Outline each blood parasite and name the species.
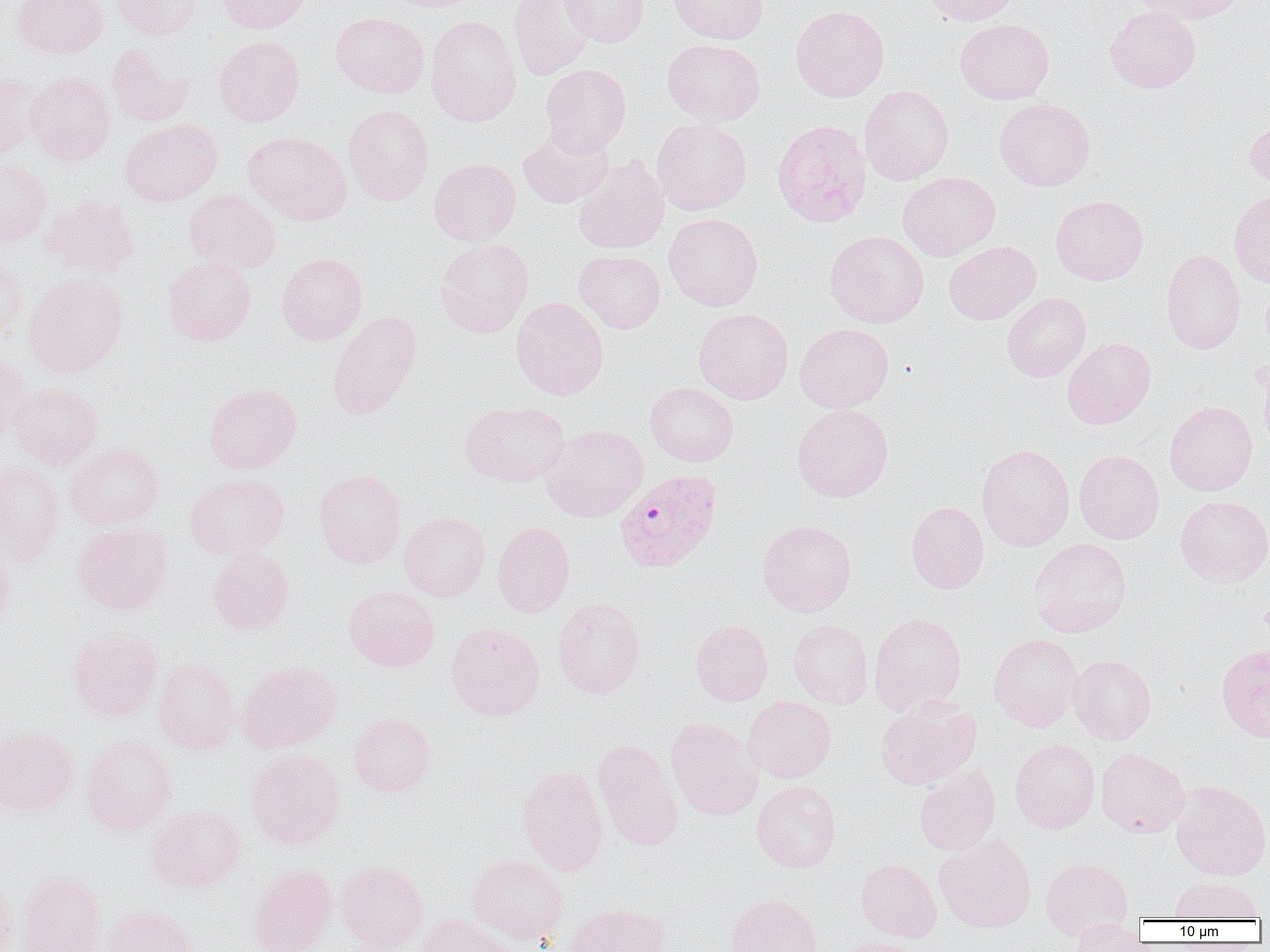
Approximate bounding boxes as (x1,y1)-(x2,y2) corner pairs in pixels.
Plasmodium falciparum-infected red blood cells: (615,469)-(722,573).
No Plasmodium ovale, Plasmodium malariae, Plasmodium vivax, Babesia divergens, or Trypanosoma brucei observed.

Uninfected red blood cell locations: (12,0)-(109,58), (112,0)-(203,40), (214,0)-(312,33), (378,0)-(481,12), (509,0)-(597,80), (560,0)-(650,47), (669,0)-(769,44), (919,0)-(1020,26), (1131,0)-(1248,24), (790,5)-(890,102), (1104,6)-(1201,93), (330,12)-(428,98), (425,15)-(521,126), (955,19)-(1054,104), (214,36)-(304,126), (662,38)-(765,126), (107,43)-(193,127), (540,63)-(631,156), (25,72)-(115,166), (0,73)-(44,160), (859,84)-(954,185), (994,97)-(1095,191), (343,104)-(434,205), (1244,115)-(1270,193), (119,118)-(222,206), (771,118)-(871,228), (652,119)-(752,215), (243,131)-(352,225), (517,131)-(614,208), (573,156)-(670,254), (429,158)-(521,246), (0,159)-(51,248), (897,171)-(1000,261), (183,189)-(281,275), (1229,192)-(1270,288), (41,195)-(139,278), (1050,195)-(1148,285), (664,213)-(763,311), (824,230)-(929,328), (434,238)-(534,337), (944,241)-(1041,324), (1161,249)-(1246,354), (574,250)-(665,333), (0,252)-(27,341), (276,252)-(367,344), (163,256)-(256,346), (23,272)-(128,378), (1002,292)-(1091,381), (511,296)-(609,400), (694,308)-(793,404), (326,310)-(423,420), (794,323)-(894,413), (1062,337)-(1156,429), (0,351)-(32,444), (1257,355)-(1270,459), (204,382)-(302,474), (645,382)-(739,466), (9,383)-(102,469), (460,400)-(569,486), (1164,401)-(1258,496), (792,403)-(894,502), (540,424)-(649,521), (67,443)-(164,529), (976,444)-(1075,551), (1074,449)-(1164,544), (0,460)-(65,566), (314,468)-(407,569), (185,473)-(290,560), (1175,495)-(1270,585), (905,501)-(989,594), (399,512)-(491,601), (757,519)-(857,616), (493,521)-(575,617), (72,522)-(172,615), (0,538)-(15,634), (1029,538)-(1132,637), (208,547)-(294,635), (344,586)-(440,671), (551,597)-(646,699), (868,612)-(967,714), (690,619)-(773,705), (788,619)-(873,708), (446,622)-(545,720), (68,627)-(164,721), (988,633)-(1082,731), (1216,643)-(1270,743), (1068,654)-(1156,744), (153,657)-(240,755), (235,660)-(342,753), (743,696)-(837,783), (875,697)-(982,791), (349,713)-(435,796), (664,717)-(763,820), (0,727)-(78,817), (80,735)-(177,835), (592,738)-(684,851), (1010,738)-(1100,833), (1095,747)-(1190,837), (246,749)-(345,848), (914,763)-(1001,856), (517,765)-(608,876), (751,780)-(841,872), (1170,780)-(1270,880), (147,806)-(246,893), (934,833)-(1037,933), (467,854)-(568,943), (1040,857)-(1133,941), (855,859)-(942,942), (336,861)-(429,952), (248,863)-(337,952), (16,870)-(106,952), (0,871)-(17,952), (1169,877)-(1263,921), (725,894)-(822,952), (564,903)-(668,952), (102,905)-(197,952), (419,914)-(518,952), (1070,919)-(1146,952), (837,937)-(928,952). Slide-level diagnosis: Plasmodium falciparum. One field of a larger specimen. Captured at 1000x magnification. Thin blood smear. Image is 1270×952 pixels. Optical microscopy.